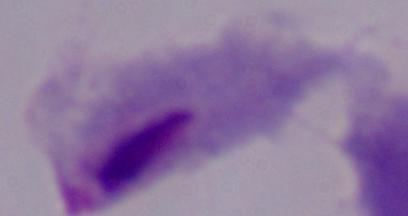

A trichomonad is seen. Micrograph. 1000x magnification.